Report the malaria status.
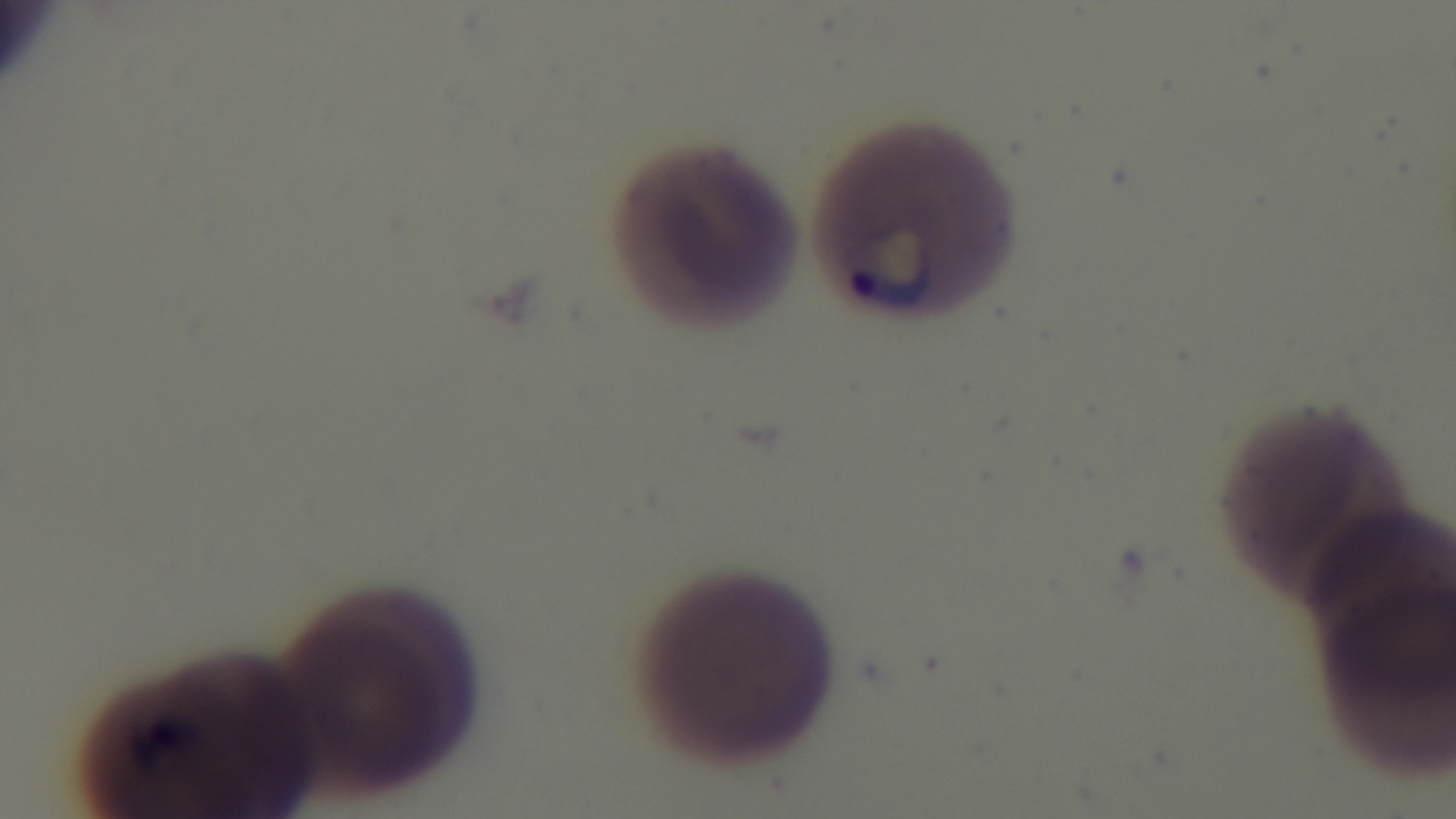
Infected.

One field from the slide. Preparation: thin. Light microscopy. Mounted 4K digital camera. 100x oil-immersion objective. Giemsa-stained.